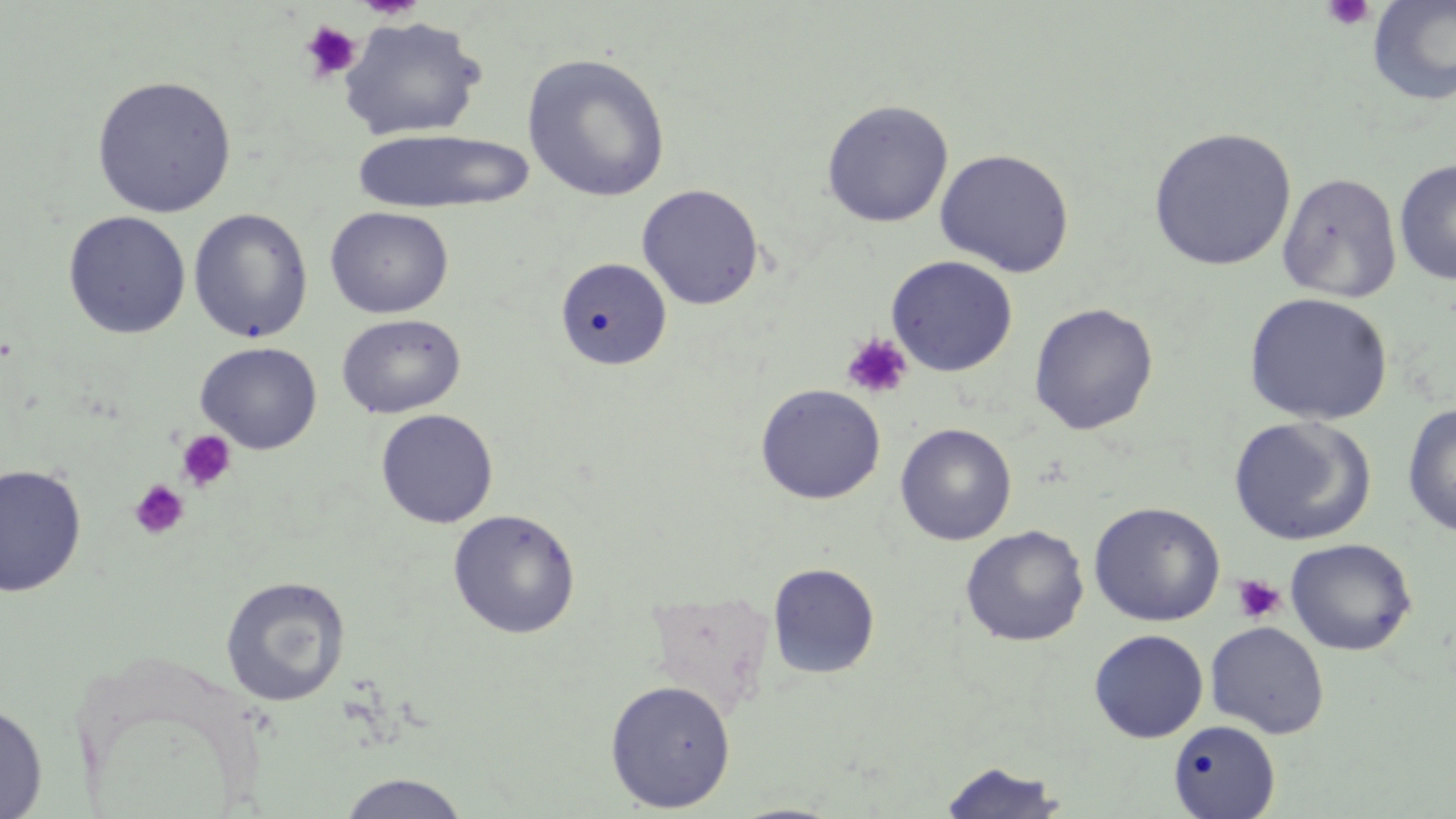

slide_level_diagnosis: negative for blood parasites
modality: light microscopy
preparation: thin blood smear
stain: May-Grünwald-Giemsa
magnification: 1000x
uninfected_red_blood_cell_locations_subset: 'approximate bounding boxes as (x1,y1)-(x2,y2) corner pairs in pixels: (1367,0)-(1456,106), (338,16)-(487,141), (521,53)-(671,203), (91,75)-(237,218), (821,99)-(954,228), (1148,127)-(1297,271), (351,129)-(534,214), (934,148)-(1075,277), (1394,159)-(1456,287), (1277,171)-(1403,304), (636,183)-(764,310), (325,206)-(453,319), (188,208)-(313,344), (63,211)-(191,339), (885,255)-(1018,377), (554,257)-(671,371), (1243,292)-(1393,426), (1028,303)-(1159,435), (336,314)-(465,419), (194,341)-(322,454), (1402,402)-(1456,536), (375,408)-(499,528), (1229,416)-(1376,545), (895,423)-(1017,546), (0,463)-(87,597), (1089,501)-(1225,627), (447,508)-(581,639), (960,525)-(1089,646), (1284,538)-(1417,656), (767,563)-(880,680), (219,575)-(352,707), (644,590)-(776,716), (1205,621)-(1330,738), (1088,629)-(1209,743), (604,679)-(736,812), (0,698)-(48,818), (1168,719)-(1281,819), (937,759)-(1067,819), (335,773)-(472,818)'
platelet_locations_subset: 'approximate bounding boxes as (x1,y1)-(x2,y2) corner pairs in pixels: (1321,0)-(1376,32), (299,20)-(362,82), (841,332)-(913,400), (176,430)-(237,492), (128,479)-(189,540), (1231,574)-(1286,624)'
field_of_view: single
image_size: 1456×819 pixels